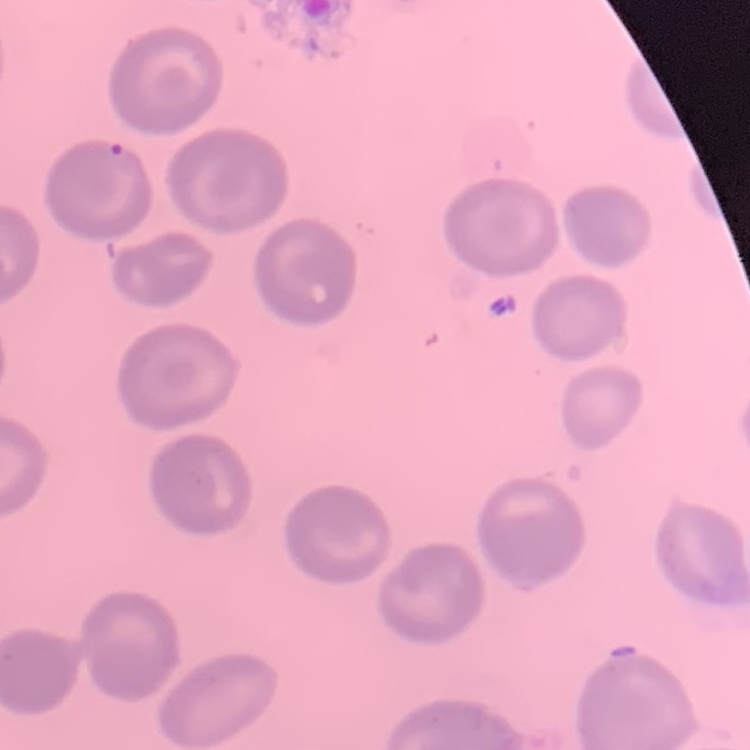
The red blood cells exhibit no rouleaux formation. Stained with either Field's or Giemsa. Square crop of a larger photomicrograph. Thin blood smear.